Assess this cell for malaria.
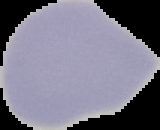

It is uninfected.

preparation = thin blood smear
image type = segmented cell region with the area outside set to black
image size = 160×130 pixels